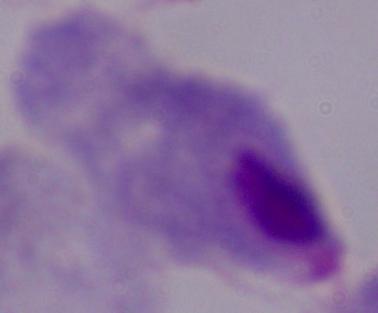

Summary:
  - Magnification: 1000x
  - Modality: micrograph
  - Identification: trichomonad